Classify this cell by malaria status.
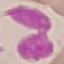

It is uninfected.

Automatically extracted cell patch, resized to 64 × 64 pixels. Giemsa stain. Thin smear of blood. Acquired by smartphone through the microscope eyepiece.